Identify the parasite.
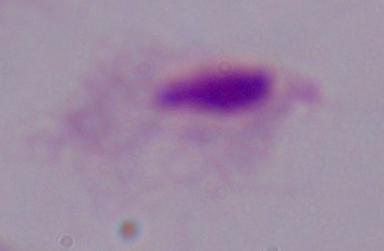
A trichomonad.

Summary:
  - Magnification: 1000x
  - Modality: photomicrograph